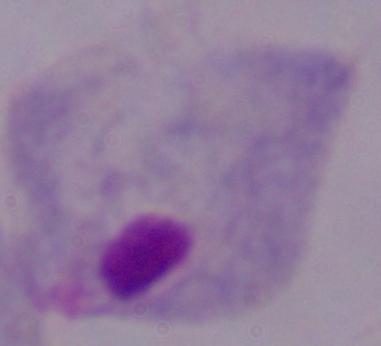
{
  "magnification": "1000x",
  "identification": "trichomonad",
  "modality": "micrograph"
}